Give the position of every Plasmodium parasite visible.
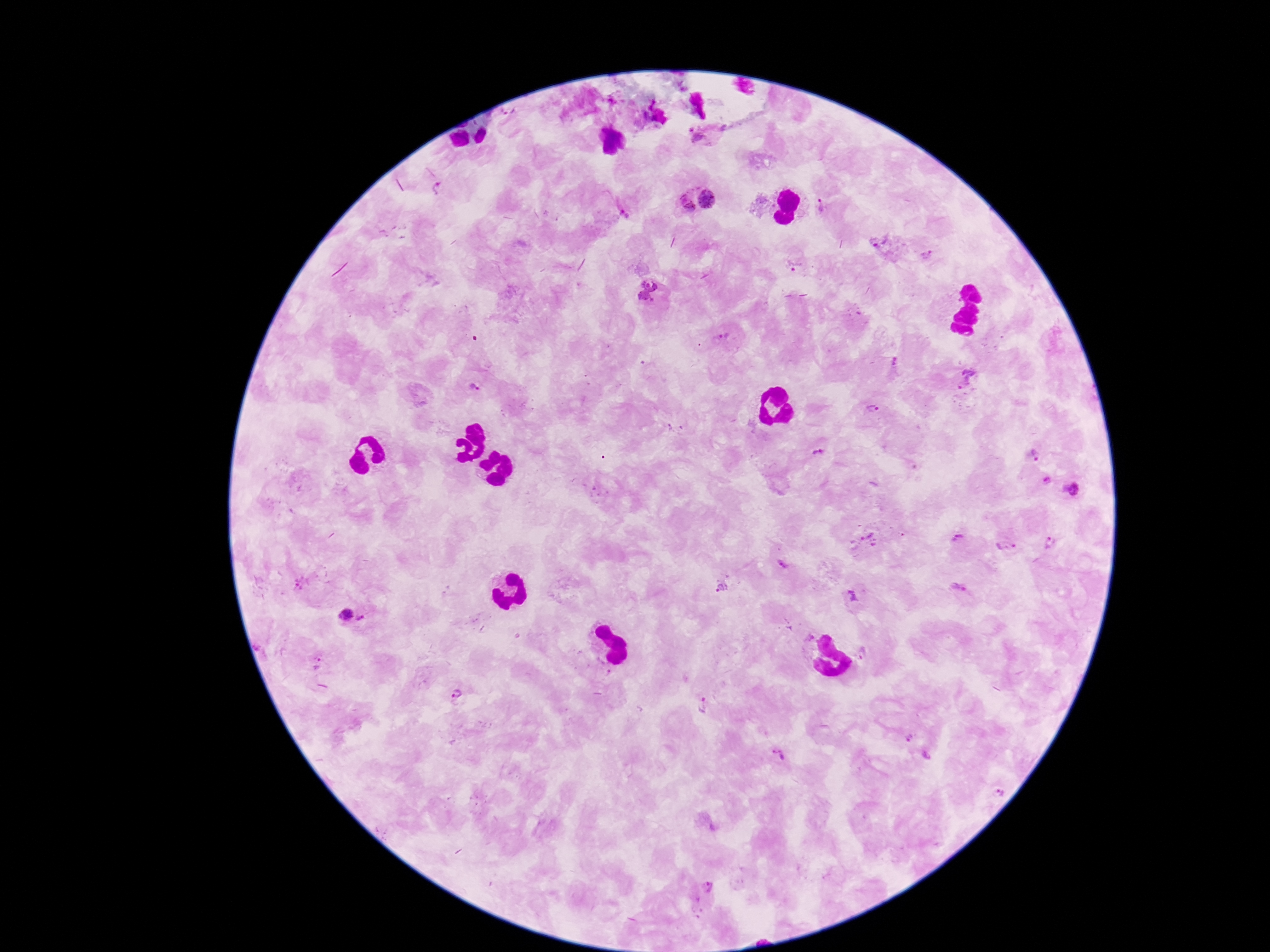

Approximate centers as {x, y} in pixels.
Plasmodium parasites: {697, 138}, {438, 188}, {708, 199}, {684, 204}, {824, 207}, {625, 211}, {929, 256}, {795, 266}, {648, 290}, {724, 336}, {896, 364}, {968, 377}, {472, 390}, {874, 409}, {819, 453}, {1035, 455}, {1046, 480}, {1073, 490}, {959, 539}, {870, 541}, {1005, 546}, {1049, 547}, {783, 565}, {723, 586}, {958, 589}, {855, 594}, {344, 614}, {362, 620}, {866, 653}, {319, 662}, {455, 694}, {703, 706}, {910, 737}, {778, 755}, {927, 756}, {707, 889}.

100x magnification. Patient malaria status: infected. Thick peripheral-blood smear. Single field of view. Smartphone photograph taken through the microscope eyepiece. Giemsa stain. Image is 1270×952 pixels.